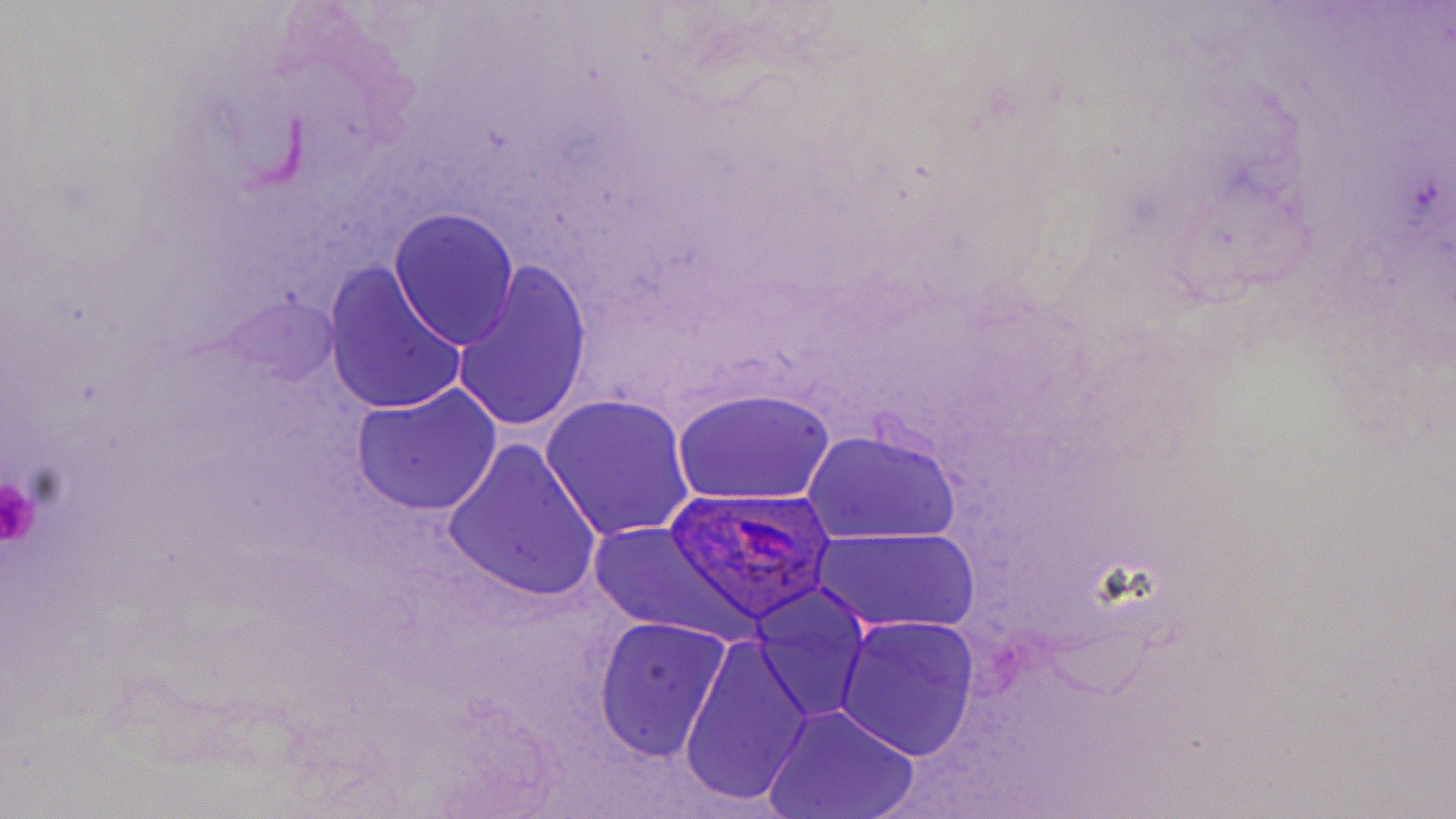

slide-level diagnosis = Plasmodium ovale
image size = 1456×819 pixels
platelet locations = approximate bounding boxes as named x1/y1/x2/y2 corners in pixels: (x1=0, y1=474, x2=41, y2=547)
preparation = thin blood film
field of view = single
magnification = 1000x
modality = light microscopy
uninfected red blood cell locations = approximate bounding boxes as named x1/y1/x2/y2 corners in pixels: (x1=389, y1=208, x2=520, y2=349), (x1=451, y1=263, x2=592, y2=436), (x1=324, y1=266, x2=467, y2=417), (x1=227, y1=291, x2=337, y2=389), (x1=350, y1=384, x2=503, y2=516), (x1=671, y1=387, x2=837, y2=509), (x1=540, y1=394, x2=698, y2=544), (x1=804, y1=430, x2=963, y2=547), (x1=442, y1=442, x2=601, y2=604), (x1=585, y1=519, x2=766, y2=643), (x1=812, y1=525, x2=982, y2=637), (x1=751, y1=583, x2=871, y2=723), (x1=834, y1=615, x2=981, y2=761), (x1=594, y1=618, x2=733, y2=763), (x1=679, y1=637, x2=814, y2=808), (x1=765, y1=705, x2=920, y2=819)
stain = May-Grünwald-Giemsa
Plasmodium ovale-infected red blood cell locations = approximate bounding boxes as named x1/y1/x2/y2 corners in pixels: (x1=660, y1=487, x2=840, y2=623)